Point out each malaria parasite.
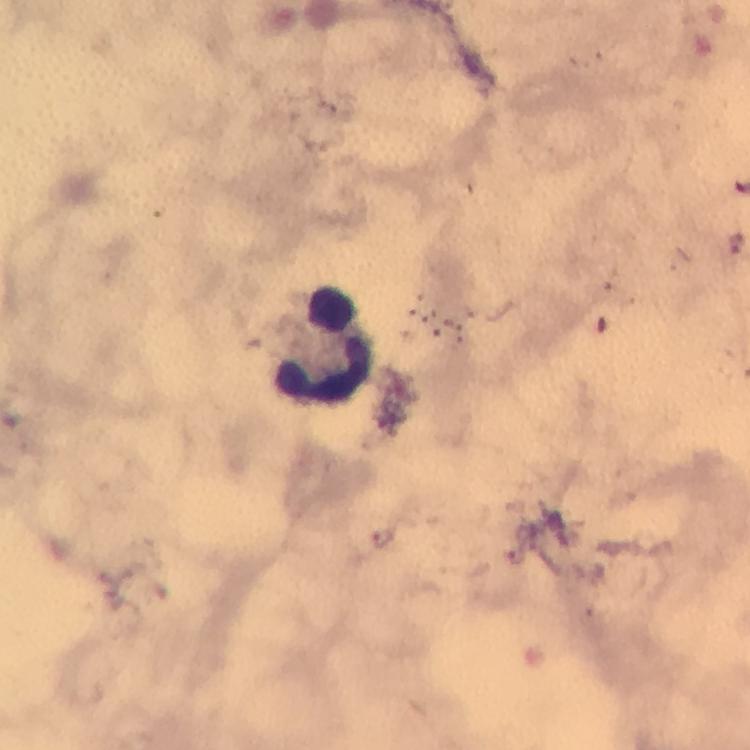
Approximate centers as [x, y] in pixels.
Malaria parasites: [384, 536], [517, 558].

Leukocyte locations: [325, 345]. Thick smear. Image is 750×750 pixels. Photographed with a smartphone mounted on the microscope. Immersion oil was used. From a diagnostic examination for malaria. Giemsa stain. 100x magnification. A crop from one field of view.